Report the malaria status of this cell.
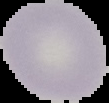
It is uninfected.

Summary:
  - Image size: 109×103 pixels
  - Image type: cell region segmented out of the field of view; surrounding area masked to black
  - Preparation: thin blood smear